Point out each Plasmodium parasite.
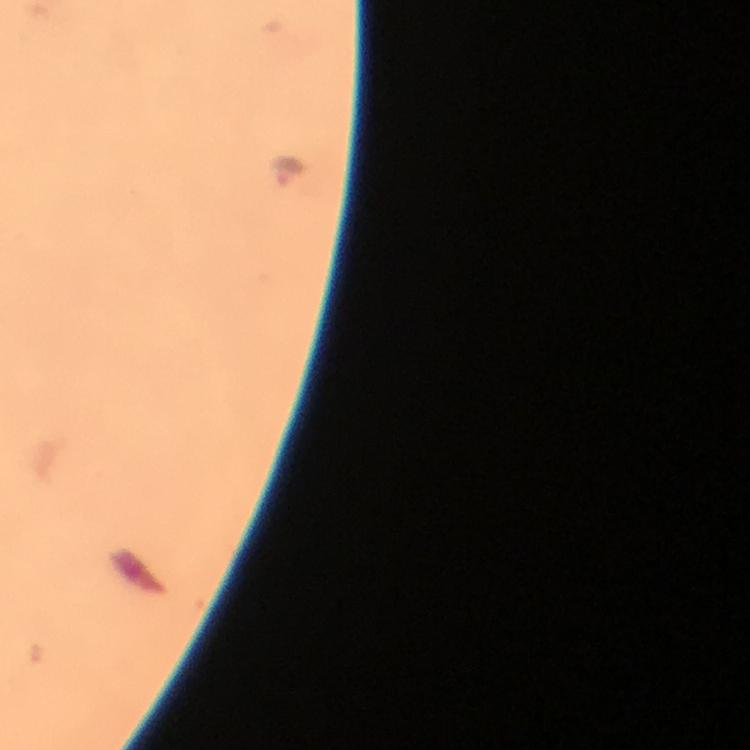

Approximate centers as {x, y} in pixels.
Plasmodium parasites: {287, 168}.

image size = 750×750 pixels
immersion oil = used
capture = smartphone camera through the microscope
magnification = 100x
cropped from = one field of view
context = from a malaria diagnostic workup
preparation = thick blood smear
stain = Giemsa